Classify this cell by malaria status.
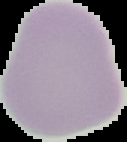
Uninfected.

preparation = thin blood film
image type = segmented cell region on a black background
image size = 127×142 pixels